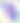

Summary:
  - Magnification: 400x
  - Modality: photomicrograph
  - Identification: Toxoplasma gondii